Rate the background quality.
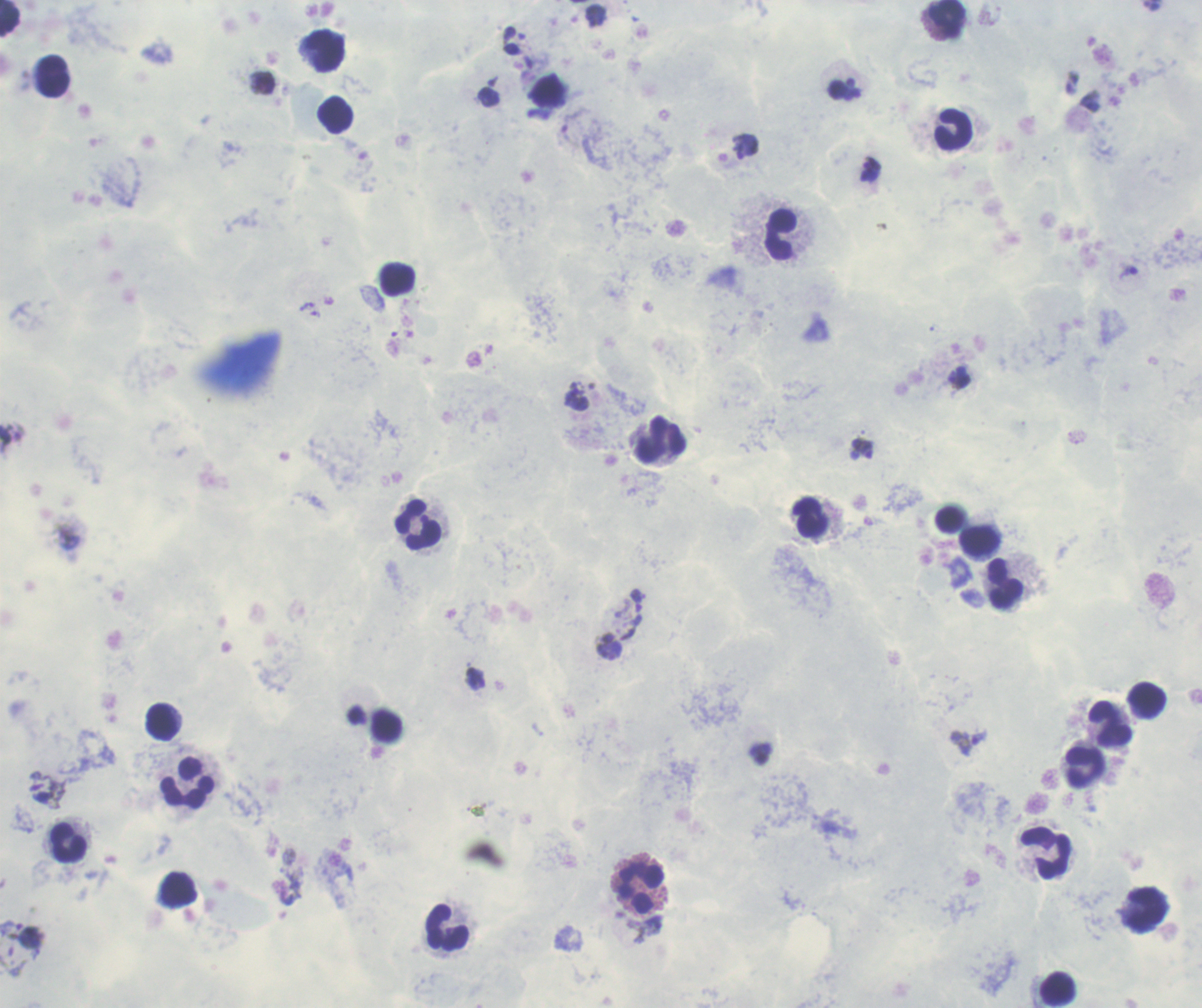
It is poor.

Approximate centers as (x, y) in pixels. Leukocyte locations: (949, 18), (325, 51), (53, 76), (335, 115), (954, 129), (780, 234), (659, 439), (810, 518), (949, 518), (418, 525), (980, 541), (1004, 583), (1147, 700), (162, 723), (1110, 726), (1086, 767), (188, 781), (68, 843), (1046, 853), (641, 888), (1145, 910), (448, 928), (1059, 989). Trophozoite locations: (1128, 272), (861, 448), (637, 601), (968, 742). Romanowsky stain. Captured at 100x magnification. Coloration quality: good. Result: positive for Plasmodium parasites. Image is 1202×1008 pixels. One field from this slide. Previously used in a real diagnosis. Thick blood film.